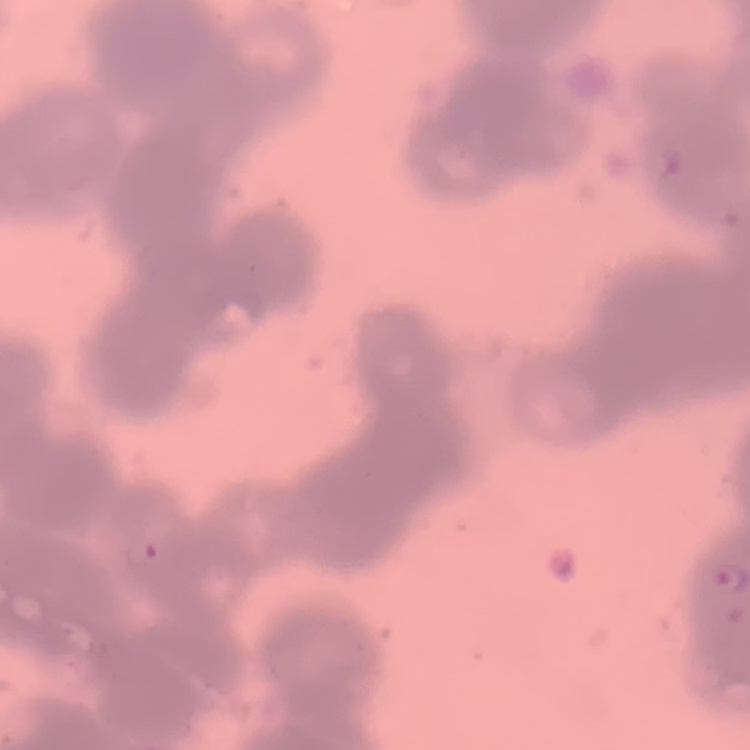
Summary:
  - Red blood cell morphology: rouleaux formation
  - Preparation: thin blood film
  - Stain: Field's or Giemsa
  - Image type: square crop of a larger photomicrograph